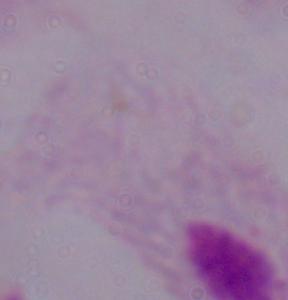
{
  "identification": "trichomonad",
  "modality": "micrograph",
  "magnification": "1000x"
}